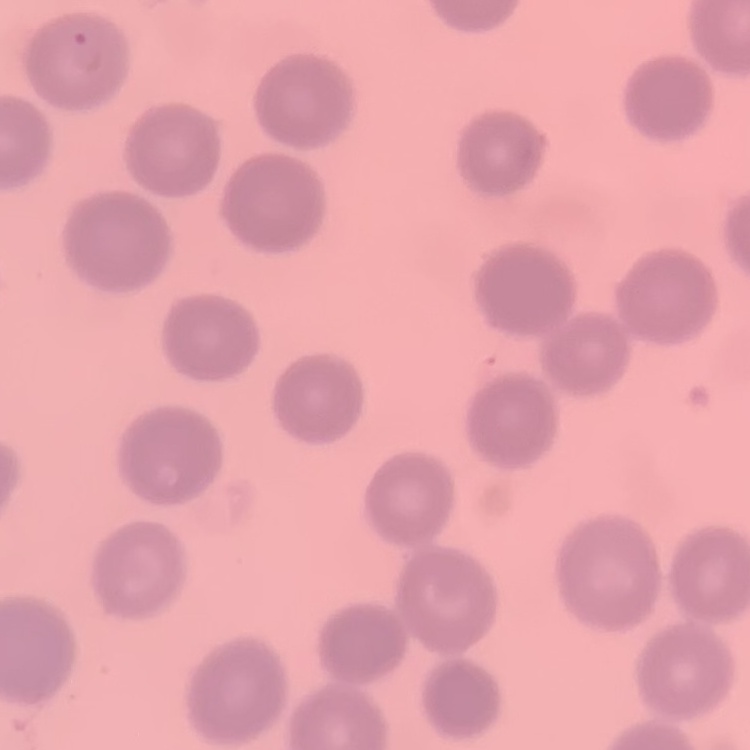
Summary:
  - Erythrocyte morphology: no rouleaux formation
  - Image type: square crop of a larger photomicrograph
  - Preparation: thin blood film
  - Stain: Field's or Giemsa